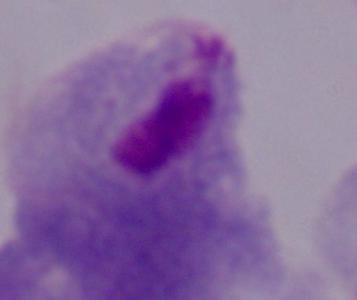
Summary:
  - Modality: photomicrograph
  - Identification: trichomonad
  - Magnification: 1000x